Assess this cell for malaria.
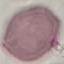
It is uninfected.

Photographed with a smartphone camera at the microscope eyepiece. Giemsa-stained preparation. Thin blood smear. Automatically extracted cell patch, resized to 64 × 64 pixels.